Classify this cell by malaria status.
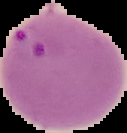

It is parasitized.

preparation: thin blood film
image_size: 127×133 pixels
image_type: segmented cell region on a black background